Outline each blood parasite and name the species.
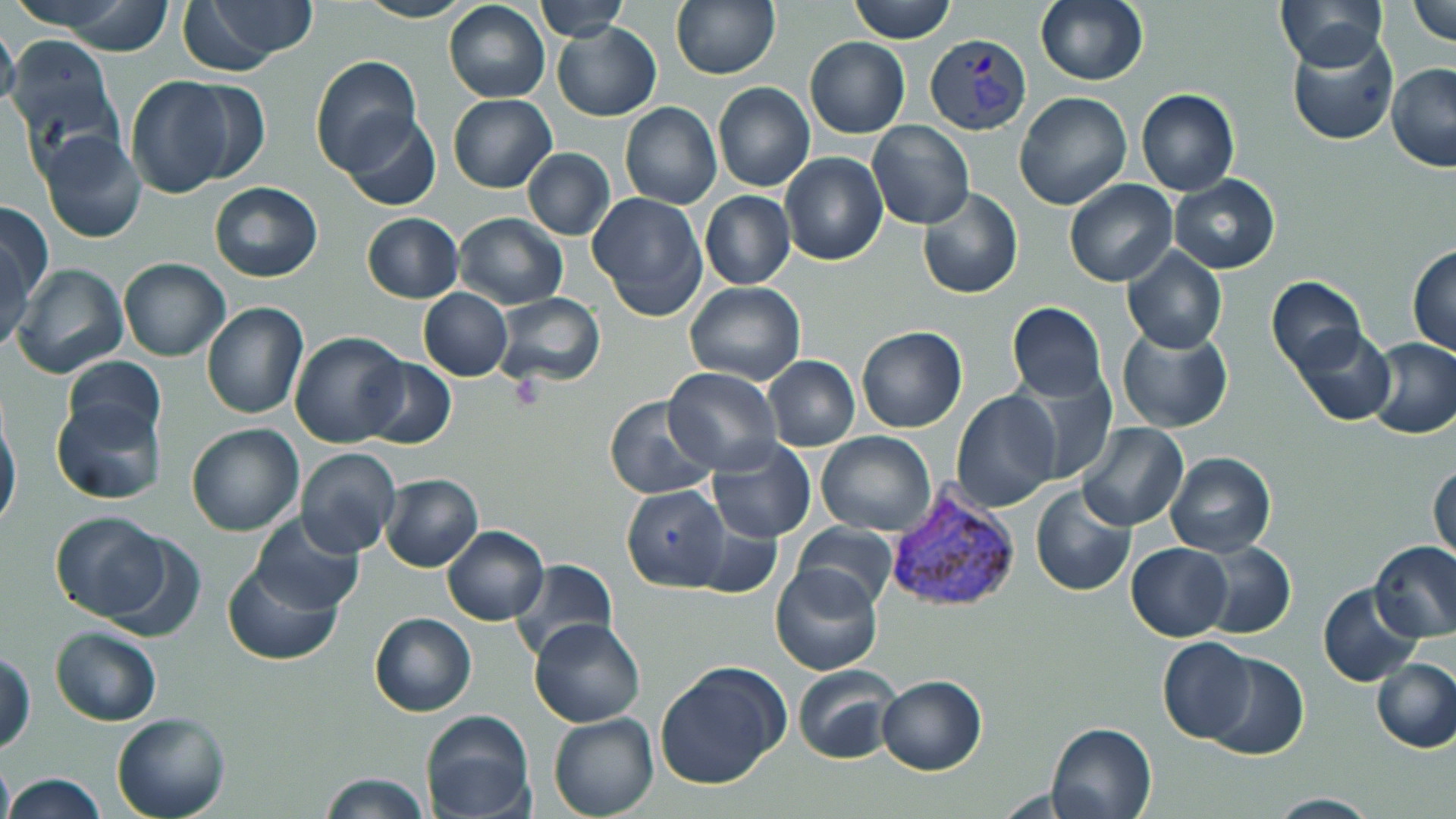
Approximate bounding boxes as (x1,y1)-(x2,y2) corner pairs in pixels.
Plasmodium vivax-infected red blood cells: (925,32)-(1032,136), (884,489)-(1021,614).
No Plasmodium falciparum, Plasmodium ovale, Plasmodium malariae, Babesia divergens, or Trypanosoma brucei observed.

slide-level diagnosis = Plasmodium vivax
image size = 1456×819 pixels
field of view = single
modality = optical microscopy
preparation = thin blood film
stain = May-Grünwald-Giemsa
magnification = 1000x
uninfected red blood cell locations = approximate bounding boxes as (x1,y1)-(x2,y2) corner pairs in pixels: (183,0)-(314,75), (536,0)-(629,41), (670,0)-(779,80), (847,0)-(959,43), (1035,0)-(1148,87), (1277,0)-(1388,71), (1408,0)-(1456,47), (52,1)-(175,56), (357,1)-(473,23), (443,1)-(551,103), (0,14)-(20,116), (552,23)-(661,120), (1286,32)-(1399,147), (6,34)-(120,157), (804,37)-(910,138), (309,55)-(421,174), (1386,63)-(1456,172), (124,78)-(239,197), (178,78)-(271,185), (712,83)-(815,193), (1136,88)-(1239,197), (1013,92)-(1131,210), (447,93)-(556,193), (619,101)-(722,209), (340,111)-(441,212), (866,122)-(975,230), (40,131)-(147,244), (522,148)-(614,238), (779,152)-(888,266), (1170,174)-(1280,275), (1065,180)-(1178,287), (208,182)-(323,282), (917,188)-(1024,300), (700,191)-(796,290), (587,192)-(708,321), (0,198)-(51,315), (454,212)-(568,309), (361,213)-(463,303), (0,234)-(34,355), (1407,244)-(1456,359), (1121,246)-(1228,355), (118,257)-(230,361), (10,263)-(129,379), (1266,276)-(1366,377), (683,281)-(806,385), (418,288)-(512,381), (495,293)-(604,388), (202,302)-(308,419), (1007,302)-(1109,402), (1116,324)-(1233,433), (856,325)-(967,433), (1290,327)-(1397,426), (289,329)-(410,449), (1363,337)-(1456,439), (63,356)-(166,446), (764,356)-(860,451), (358,358)-(455,449), (662,366)-(781,474), (1011,370)-(1120,485), (950,390)-(1062,512), (602,395)-(719,501), (52,397)-(165,505), (0,409)-(21,535), (186,422)-(304,536), (1076,422)-(1188,532), (817,431)-(936,536), (705,438)-(815,544), (295,447)-(399,557), (1166,451)-(1276,557), (1430,460)-(1455,564), (380,474)-(484,572), (622,484)-(730,592), (1031,485)-(1138,598), (49,511)-(169,621), (249,512)-(364,615), (690,515)-(783,598), (793,523)-(900,612), (441,525)-(548,625), (96,531)-(206,642), (1195,540)-(1296,640), (1370,541)-(1456,641), (1126,542)-(1233,641), (510,559)-(616,660), (223,561)-(343,665), (770,563)-(883,676), (1317,582)-(1424,687), (369,612)-(477,717), (530,617)-(645,727), (49,626)-(162,726), (1157,637)-(1257,744), (1202,651)-(1307,761), (0,652)-(36,755), (1370,656)-(1456,754), (654,661)-(792,790), (792,664)-(901,765), (876,676)-(987,775), (420,709)-(537,819), (111,710)-(230,819), (548,714)-(659,819), (1046,720)-(1159,819), (0,751)-(13,819), (319,773)-(431,818), (3,774)-(106,818), (1260,793)-(1385,818)